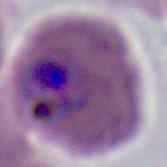
{
  "magnification": "400x or 1000x",
  "identification": "Plasmodium",
  "modality": "photomicrograph"
}